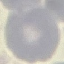 Malaria status: uninfected. Thin blood smear. Acquired by smartphone through the microscope eyepiece. Automatically extracted cell patch, resized to 64 × 64 pixels. Giemsa stain.